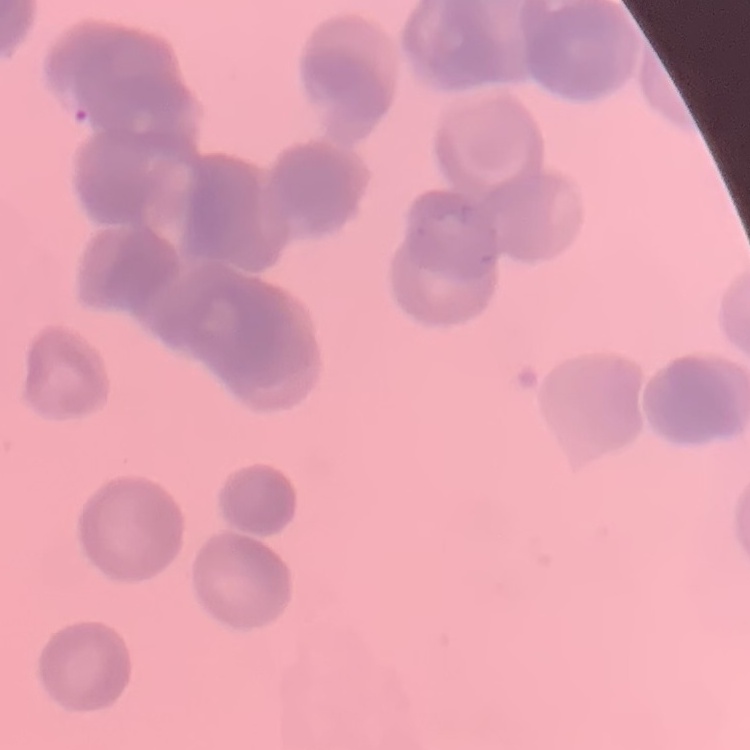

red blood cell morphology = rouleaux formation
image type = one tile cut from a larger photomicrograph
preparation = thin blood smear
stain = Field's or Giemsa